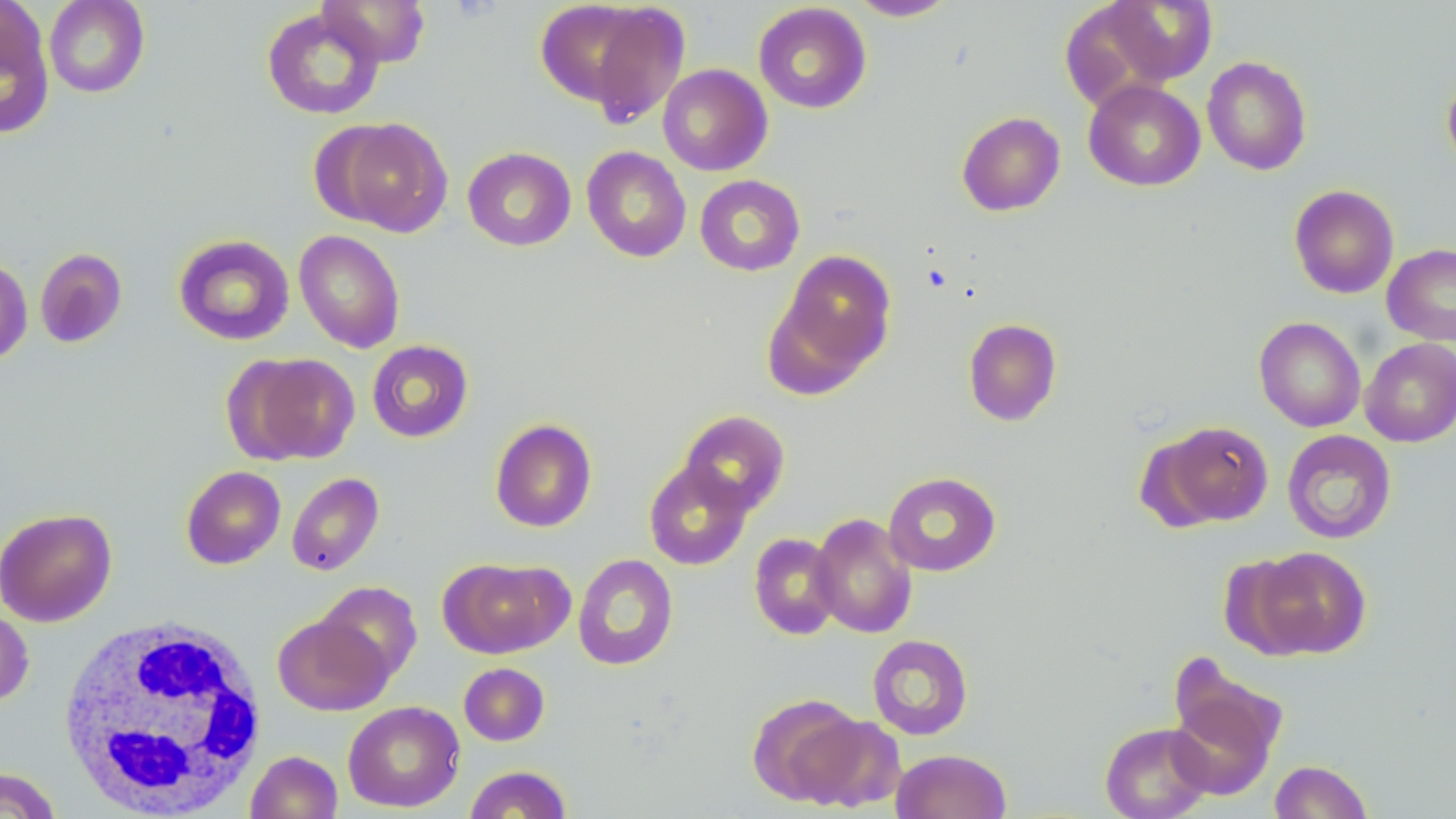

slide-level diagnosis = negative for blood parasites
uninfected red blood cell locations = approximate bounding boxes as [x1, y1, x2, y2] in pixels: [43, 0, 149, 98], [316, 0, 431, 67], [541, 0, 691, 124], [846, 0, 958, 21], [1098, 1, 1218, 87], [753, 2, 872, 114], [0, 3, 54, 138], [261, 6, 385, 121], [1201, 56, 1313, 175], [657, 63, 773, 176], [1441, 70, 1456, 175], [1083, 79, 1205, 191], [956, 111, 1066, 216], [326, 117, 453, 236], [582, 146, 691, 262], [462, 147, 576, 251], [695, 174, 805, 276], [1289, 184, 1399, 299], [294, 229, 405, 353], [173, 234, 295, 345], [1382, 243, 1456, 345], [34, 248, 128, 347], [776, 249, 897, 378], [0, 256, 32, 365], [1254, 316, 1366, 432], [963, 318, 1062, 426], [1360, 338, 1456, 447], [367, 339, 474, 443], [231, 352, 360, 465], [678, 410, 790, 516], [490, 418, 597, 532], [1153, 420, 1274, 527], [1282, 429, 1397, 544], [644, 460, 754, 571], [181, 465, 286, 569], [883, 471, 1001, 576], [287, 472, 384, 576], [0, 507, 117, 627], [809, 513, 918, 638], [748, 533, 841, 640], [1247, 546, 1372, 659], [573, 553, 678, 671], [438, 557, 572, 658], [317, 582, 422, 683], [0, 606, 34, 707], [273, 613, 392, 716], [867, 634, 974, 740], [458, 662, 550, 745], [1167, 665, 1287, 797], [747, 693, 867, 806], [342, 700, 465, 812], [797, 714, 905, 812], [1099, 722, 1214, 819], [891, 749, 1011, 819], [245, 750, 342, 818], [1269, 760, 1374, 819], [463, 765, 573, 818], [0, 767, 63, 819]
image size = 1456×819 pixels
white blood cell locations = approximate bounding boxes as [x1, y1, x2, y2] in pixels: [56, 615, 269, 817]
magnification = 1000x
field of view = single
stain = May-Grünwald-Giemsa
modality = optical microscopy
preparation = thin blood film